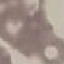 Malaria status: uninfected. Photographed with a smartphone camera at the microscope eyepiece. Giemsa stain. Thin blood smear. Cell patch, automatically extracted from a larger field of view and resized to 64 × 64 pixels.